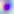

Summary:
  - Identification: Toxoplasma gondii
  - Modality: photomicrograph
  - Magnification: 400x